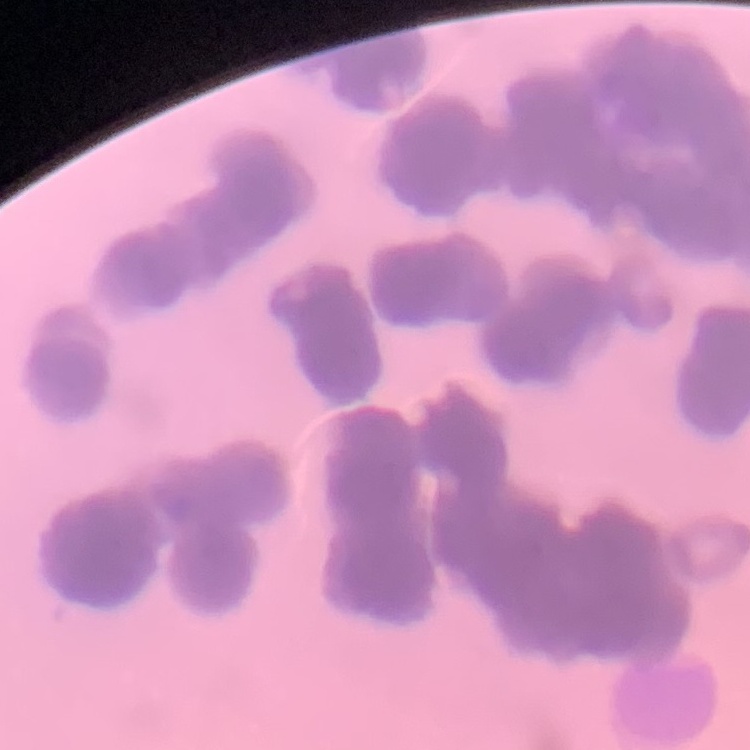

erythrocyte morphology = rouleaux formation
image type = one tile cut from a larger photomicrograph
preparation = thin blood smear
stain = Field's or Giemsa